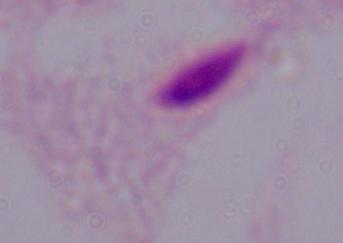
identification = trichomonad
magnification = 1000x
modality = photomicrograph